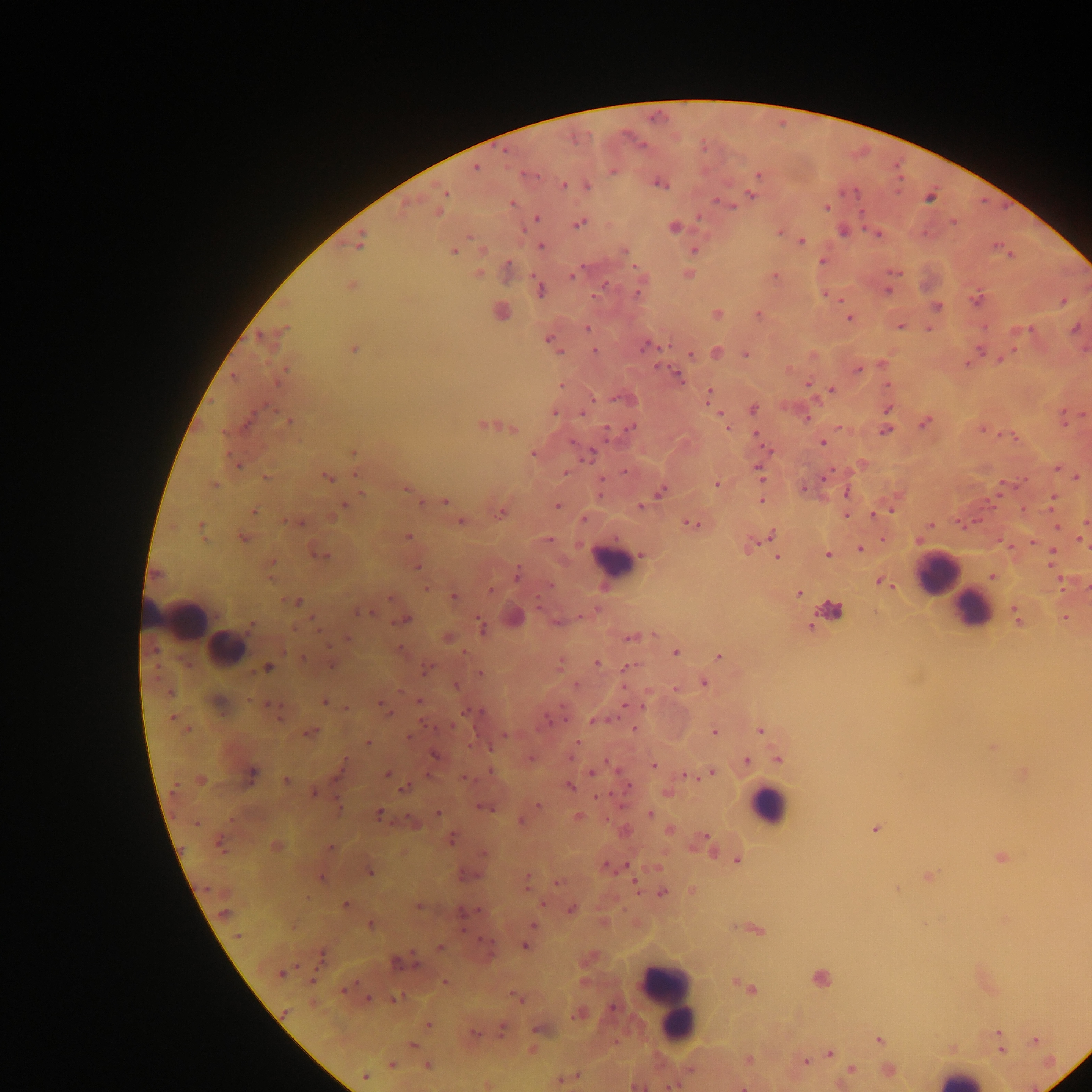
Plasmodium parasite locations = approximate centers as [x, y] in pixels: [476, 168], [613, 170], [758, 175], [564, 185], [587, 185], [660, 185], [445, 192], [854, 192], [751, 195], [930, 198], [725, 203], [512, 204], [827, 207], [440, 211], [536, 218], [954, 222], [579, 224], [674, 226], [780, 231], [844, 231], [877, 234], [802, 240], [359, 244], [540, 245], [625, 251], [694, 251], [454, 252], [822, 261], [508, 266], [895, 272], [478, 274], [688, 274], [573, 275], [774, 275], [605, 286], [352, 287], [541, 290], [637, 292], [976, 299], [1063, 302], [938, 306], [501, 313], [758, 313], [717, 314], [849, 318], [901, 327], [588, 328], [1075, 328], [285, 329], [929, 329], [1030, 329], [261, 337], [549, 341], [647, 346], [354, 349], [594, 350], [979, 351], [716, 353], [690, 354], [745, 354], [1003, 358], [858, 369], [234, 377], [677, 377], [808, 384], [562, 386], [831, 389], [709, 395], [622, 398], [754, 409], [888, 409], [554, 412], [584, 413], [288, 422], [924, 422], [483, 425], [631, 427], [726, 427], [513, 429], [886, 430], [607, 432], [573, 443], [822, 443], [353, 452], [591, 453], [533, 454], [238, 464], [1057, 469], [624, 472], [758, 472], [566, 473], [326, 476], [1076, 477], [267, 478], [716, 484], [214, 485], [804, 489], [406, 490], [661, 491], [361, 492], [847, 493], [1053, 498], [761, 500], [419, 502], [445, 502], [344, 505], [557, 505], [641, 506], [253, 511], [883, 512], [500, 513], [846, 516], [584, 519], [298, 522], [461, 522], [691, 524], [930, 525], [1057, 526], [200, 528], [770, 535], [408, 537], [244, 538], [548, 540], [1082, 540], [861, 549], [642, 554], [827, 554], [320, 555], [1052, 555], [777, 558], [271, 564], [417, 567], [156, 573], [517, 575], [992, 577], [882, 583], [426, 589], [491, 591], [799, 594], [454, 596], [391, 598], [295, 601], [832, 611], [363, 613], [1016, 614], [1066, 618], [405, 620], [556, 622], [481, 628], [447, 637], [631, 637], [347, 639], [401, 649], [676, 653], [719, 657], [303, 658], [597, 663], [330, 666], [627, 666], [269, 668], [427, 669], [481, 673], [704, 683], [575, 685], [456, 686], [675, 689], [169, 693], [419, 701], [325, 702], [271, 705], [383, 707], [477, 712], [173, 718], [595, 720], [452, 726], [188, 729], [634, 729], [760, 731], [311, 732], [714, 732], [504, 735], [410, 738], [368, 744], [490, 747], [435, 755], [531, 758], [779, 759], [746, 761], [654, 765], [339, 771], [593, 771], [252, 773], [711, 773], [387, 774], [688, 776], [201, 779], [464, 779], [286, 780], [569, 787], [628, 788], [405, 789], [315, 794], [538, 804], [484, 807], [339, 808], [438, 813], [650, 813], [378, 814], [579, 817], [521, 821], [196, 823], [875, 829], [669, 831], [452, 838], [705, 838], [219, 845], [276, 846], [331, 847], [484, 853], [1001, 858], [738, 861], [607, 867], [369, 873], [528, 876], [321, 879], [558, 881], [634, 884], [662, 893], [345, 905], [419, 907], [572, 909], [462, 912], [224, 913], [370, 925], [533, 925], [237, 935], [525, 946], [440, 947], [401, 962], [281, 974], [445, 983], [751, 989], [518, 998], [369, 999], [428, 1024], [502, 1029], [999, 1032], [475, 1033], [880, 1040], [1035, 1041], [412, 1045], [1001, 1051], [830, 1053], [749, 1059], [806, 1062], [392, 1065], [428, 1066], [851, 1070], [365, 1076], [671, 1086]
field of view = single
country = Ghana
preparation = thick blood film
leukocyte locations = approximate centers as [x, y] in pixels: [611, 560], [936, 574], [973, 609], [180, 616], [226, 649], [769, 804], [669, 999], [959, 1078]
image size = 1092×1092 pixels
capture = mobile-phone photograph through a microscope